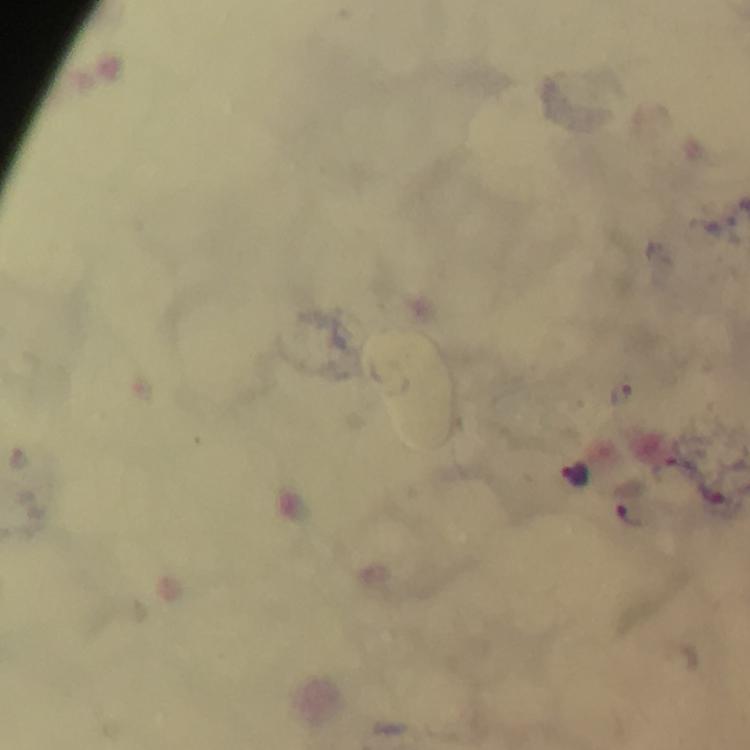
Approximate object centers, in pixels from the top-left corner. Plasmodium parasite locations: (x=622, y=396), (x=577, y=473), (x=708, y=490), (x=631, y=502). Thick blood film. Cropped region of a single field of view. Image is 750×750 pixels. Immersion oil was used. From a malaria diagnostic workup. Giemsa-stained preparation. 100x magnification. Photographed through the microscope with a smartphone camera.